Look for Plasmodium parasites.
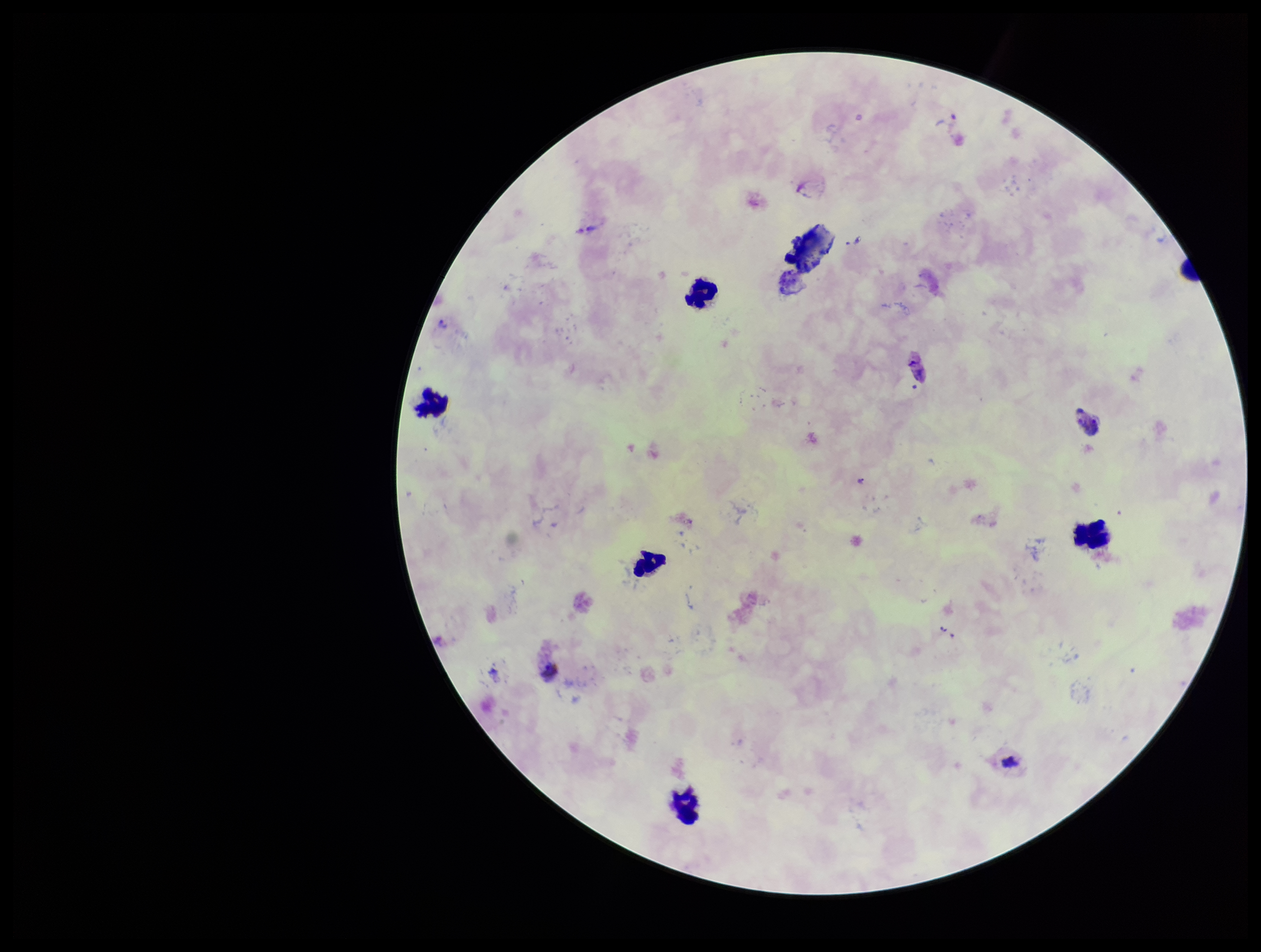
Detected.

Image is 1261×952 pixels. Single field of view. Leukocyte count: 6. Giemsa stain. Parasite count: 4. Species reported for this patient: Plasmodium vivax. Smartphone photograph taken through the eyepiece of a microscope. Preparation: thick. Patient malaria status: positive.